Comment on the morphology of the red blood cells.
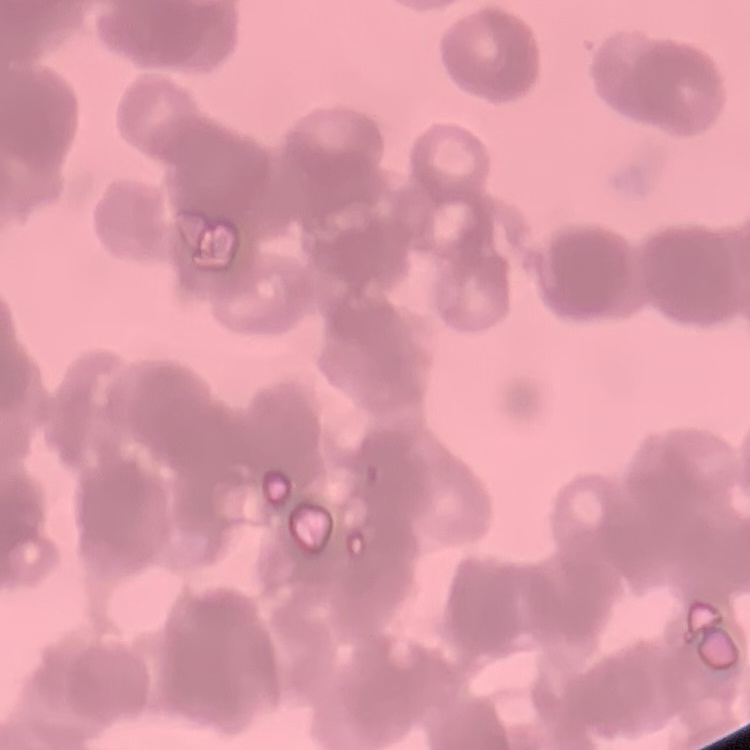

They show rouleaux formation.

preparation = thin blood film
stain = Field's or Giemsa
image type = one tile cut from a larger photomicrograph